Classify this cell by malaria status.
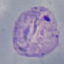

Parasitized.

Summary:
  - Stain: Giemsa
  - Capture: smartphone through the microscope eyepiece
  - Image type: automatically extracted cell patch, resized to 64 × 64 pixels
  - Preparation: thin blood film